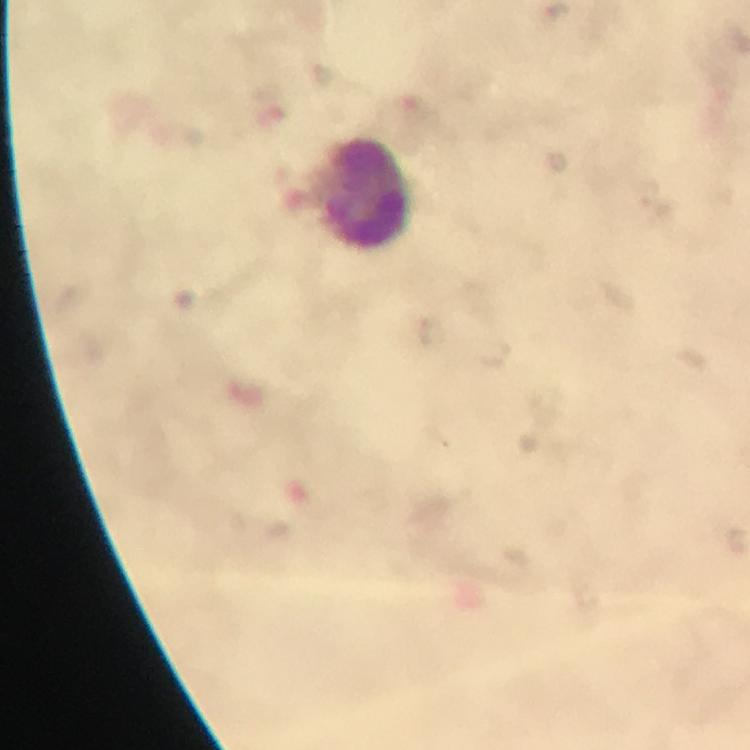 Approximate centers as {x, y} in pixels. Leukocyte locations: {363, 194}. 100x magnification. From a malaria diagnostic workup. Malaria parasites: none detected. Immersion oil was used. Thick blood smear. Giemsa stain. Cropped region of a single field of view. Smartphone photograph taken through a microscope. Image is 750×750 pixels.